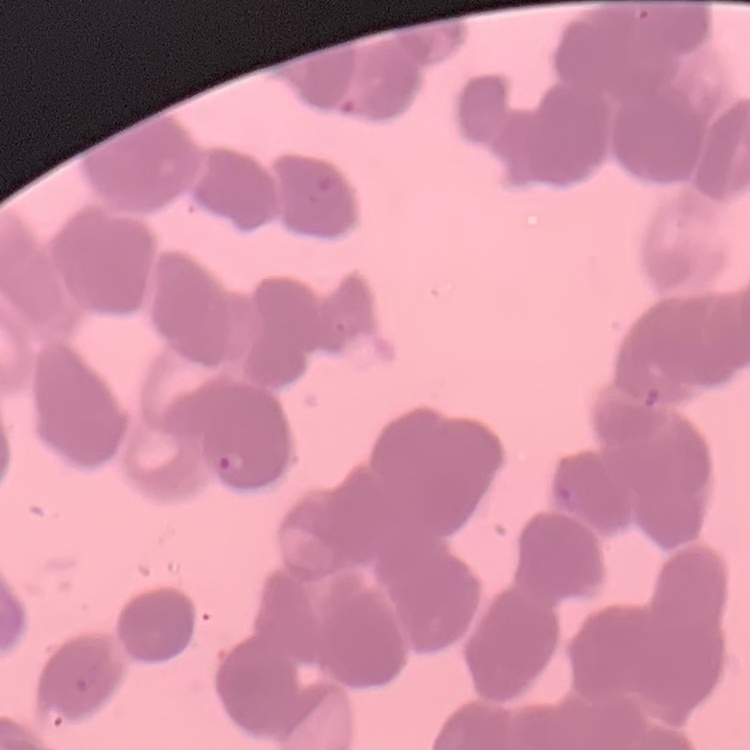

The erythrocytes show rouleaux formation. Square crop of a larger photomicrograph. Thin peripheral smear. Stained with either Field's or Giemsa.